Report the malaria status of this cell.
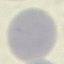

It is uninfected.

image type = cell patch, automatically extracted from a larger field of view and resized to 64 × 64 pixels
stain = Giemsa
preparation = thin blood smear
capture = smartphone through the microscope eyepiece